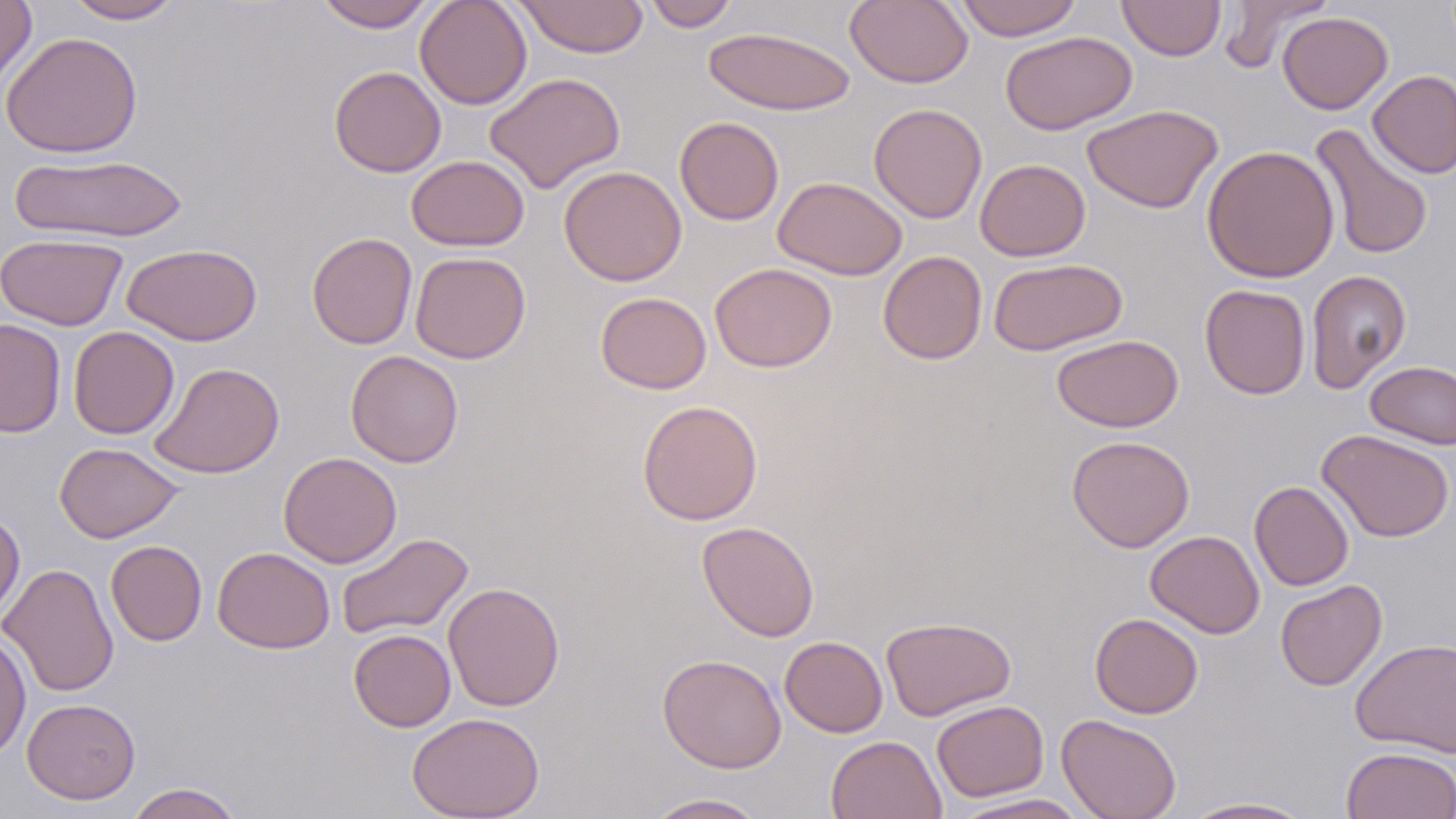
Summary:
  - Coordinate format: approximate bounding boxes as [x1, y1, x2, y2] in pixels
  - Uninfected red blood cell locations: [0, 0, 37, 91], [64, 0, 185, 24], [313, 0, 437, 31], [414, 0, 532, 110], [514, 0, 649, 58], [845, 0, 973, 89], [954, 0, 1083, 40], [1117, 0, 1226, 60], [1218, 0, 1334, 73], [642, 1, 740, 31], [1278, 11, 1393, 114], [704, 25, 856, 116], [1000, 30, 1137, 135], [0, 31, 143, 158], [329, 65, 446, 177], [1368, 69, 1456, 179], [485, 72, 626, 193], [868, 103, 988, 223], [1082, 104, 1223, 214], [674, 116, 784, 225], [1310, 124, 1434, 260], [1202, 144, 1340, 283], [8, 153, 188, 243], [406, 155, 529, 251], [975, 159, 1090, 261], [558, 166, 686, 286], [772, 176, 907, 280], [306, 231, 417, 349], [0, 233, 127, 330], [122, 243, 263, 345], [877, 250, 987, 365], [410, 251, 530, 363], [988, 257, 1127, 356], [709, 262, 837, 372], [1306, 269, 1411, 394], [1199, 284, 1310, 399], [595, 292, 711, 393], [0, 318, 67, 437], [68, 326, 179, 439], [1051, 334, 1183, 432], [346, 350, 463, 467], [1364, 360, 1456, 449], [149, 362, 285, 479], [637, 399, 763, 526], [1317, 429, 1455, 542], [1067, 434, 1195, 552], [54, 442, 183, 543], [278, 451, 402, 568], [1249, 481, 1354, 591], [0, 510, 25, 625], [697, 521, 820, 642], [1145, 530, 1265, 638], [336, 532, 474, 639], [106, 540, 207, 646], [212, 546, 335, 654], [1, 563, 119, 698], [1274, 579, 1388, 692], [443, 581, 565, 711], [1089, 612, 1204, 718], [881, 615, 1016, 721], [348, 628, 456, 731], [0, 632, 32, 761], [779, 636, 888, 738], [1350, 638, 1456, 757], [657, 653, 786, 773], [22, 698, 140, 804], [931, 699, 1049, 802], [407, 712, 545, 819], [1056, 713, 1182, 819], [826, 735, 946, 819], [1342, 747, 1456, 818], [125, 782, 245, 819], [643, 792, 770, 818], [948, 793, 1093, 819], [1178, 796, 1318, 818]
  - Slide-level diagnosis: no evidence of blood parasites
  - Stain: May-Grünwald-Giemsa
  - Magnification: 1000x
  - Field of view: single
  - Modality: light microscopy
  - Preparation: thin blood film
  - Image size: 1456×819 pixels